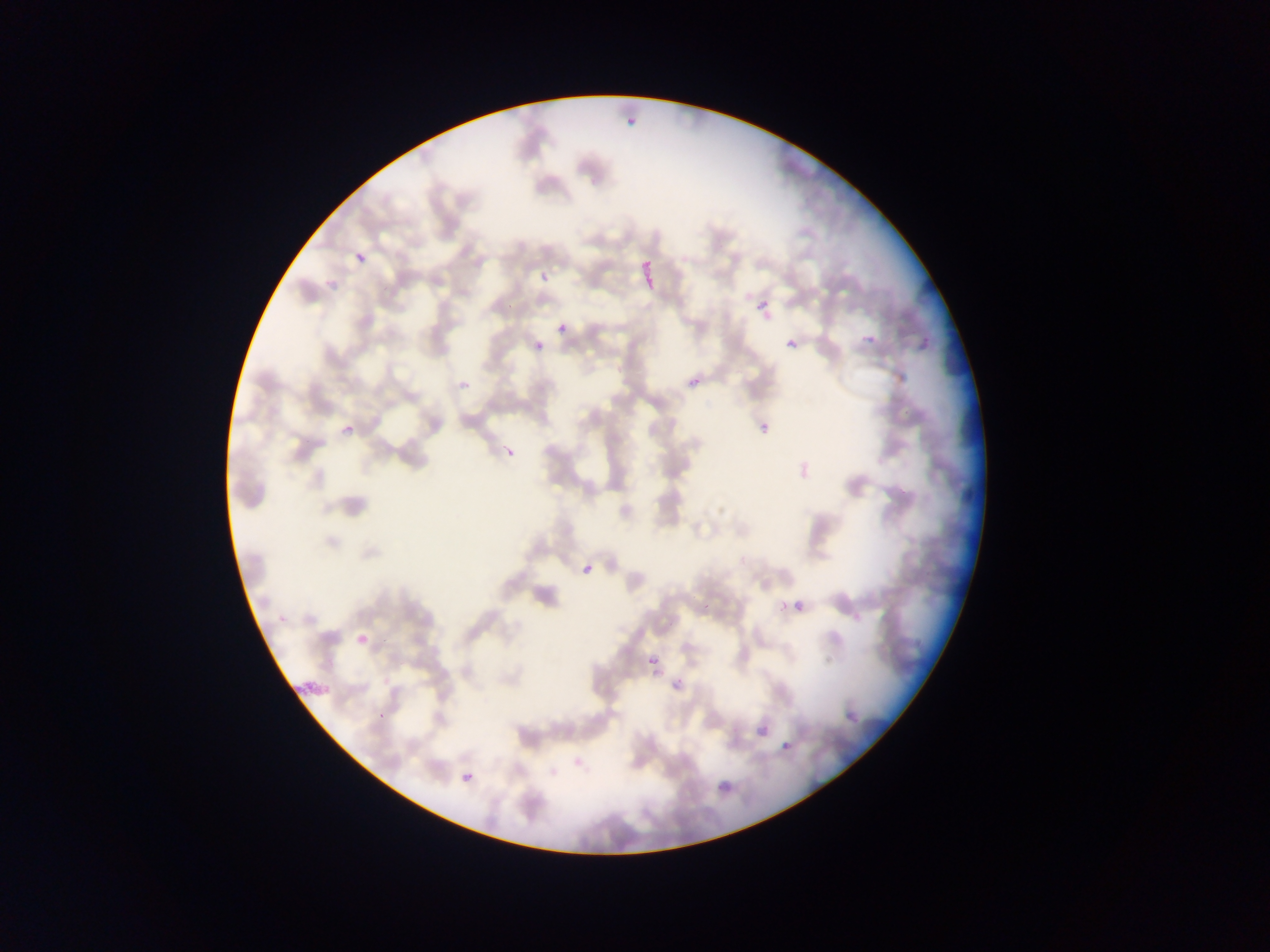
Approximate bounding boxes as {left, top, right, bottom} in pixels.
Summary:
  - Malaria parasite locations: {621, 117, 635, 133}, {354, 249, 367, 265}, {540, 272, 548, 282}, {760, 300, 770, 311}, {557, 323, 568, 335}, {863, 332, 876, 346}, {785, 339, 798, 350}, {535, 341, 544, 350}, {687, 368, 708, 390}, {459, 380, 471, 391}, {760, 422, 770, 433}, {343, 424, 356, 436}, {502, 442, 516, 454}, {580, 558, 597, 573}, {795, 601, 804, 610}, {778, 602, 787, 611}, {703, 603, 711, 611}, {648, 651, 665, 667}, {669, 669, 692, 696}, {847, 706, 858, 722}, {757, 727, 766, 737}, {783, 742, 791, 750}, {461, 772, 473, 783}, {714, 772, 737, 800}
  - Image size: 1270×952 pixels
  - Capture: mobile-phone photograph through a microscope
  - Field of view: single
  - Preparation: thin blood smear
  - Country: Ghana